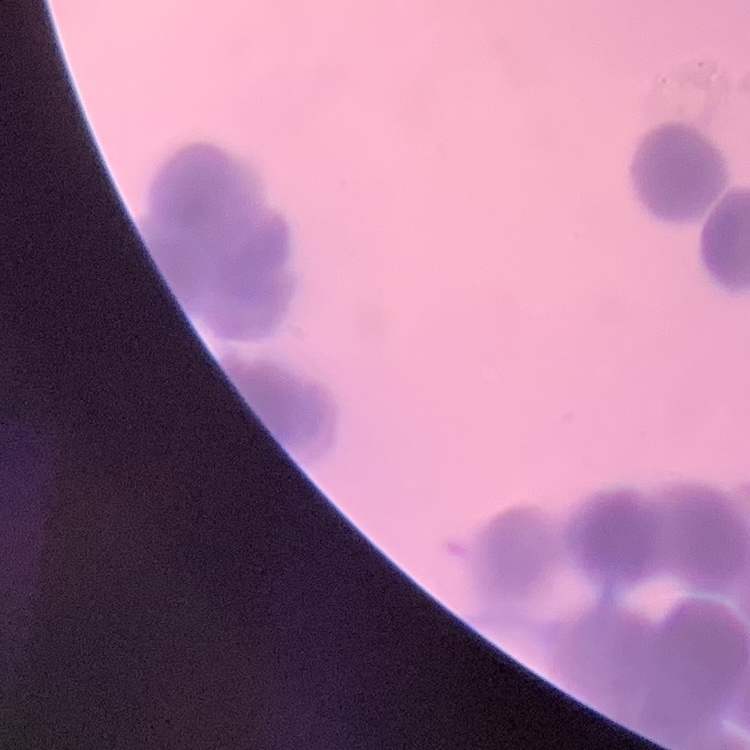 The erythrocytes show rouleaux formation. Thin blood smear. One tile cut from a larger photomicrograph. Field's or Giemsa stain.